Give the preparation type.
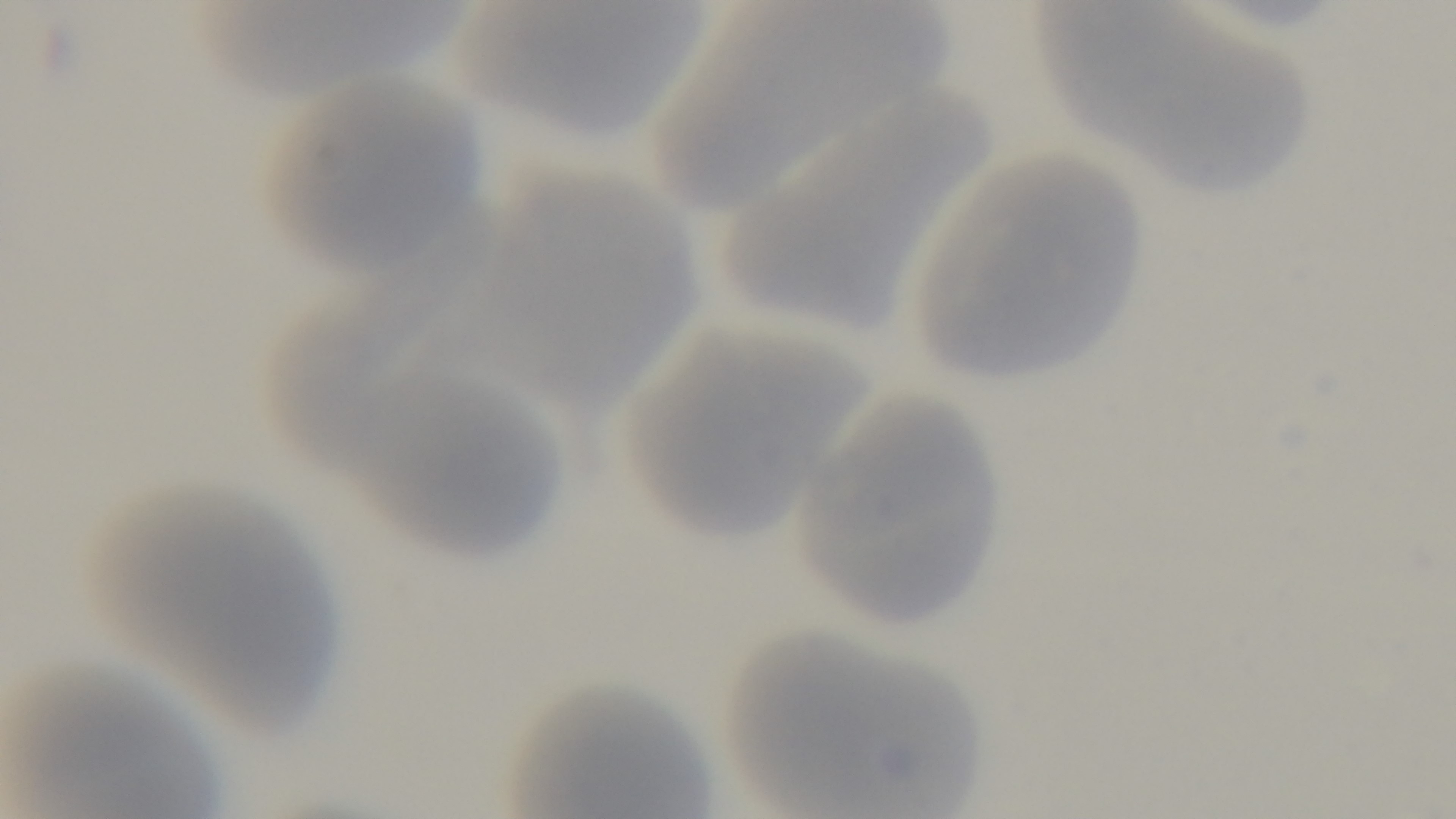

Thin.

Summary:
  - Field of view: single
  - Stain: Giemsa
  - Capture: mounted 4K digital camera
  - Malaria status: uninfected
  - Modality: light microscopy
  - Objective: 100x oil immersion